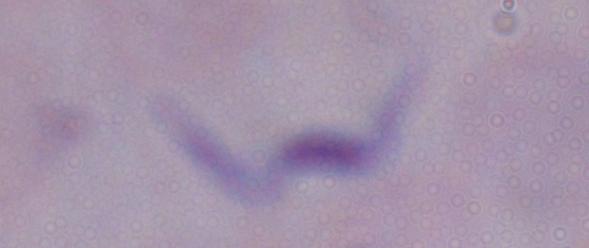
{
  "identification": "trypanosome",
  "modality": "micrograph",
  "magnification": "1000x"
}